Classify this cell by malaria status.
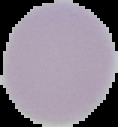

Uninfected.

Image is 118×127 pixels. From a thin blood film. The area outside the segmented cell region is set to black.